Classify this cell by malaria status.
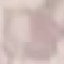

Uninfected.

Summary:
  - Preparation: thin blood smear
  - Image type: cell patch, automatically extracted from a larger field of view and resized to 64 × 64 pixels
  - Stain: Giemsa
  - Capture: smartphone camera at the microscope eyepiece